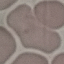

result = no malaria parasites detected
image type = automatically extracted cell patch, resized to 64 × 64 pixels
stain = Giemsa
capture = smartphone camera at the microscope eyepiece
preparation = thin blood film